Classify this cell by malaria status.
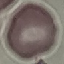
Uninfected.

preparation = thin blood smear
capture = smartphone camera at the microscope eyepiece
image type = cell patch, automatically extracted from a larger field of view and resized to 64 × 64 pixels
stain = Giemsa